Assess this cell for malaria.
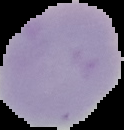
Uninfected.

Summary:
  - Image size: 124×130 pixels
  - Preparation: thin blood smear
  - Image type: cell region segmented out of the field of view; surrounding area masked to black